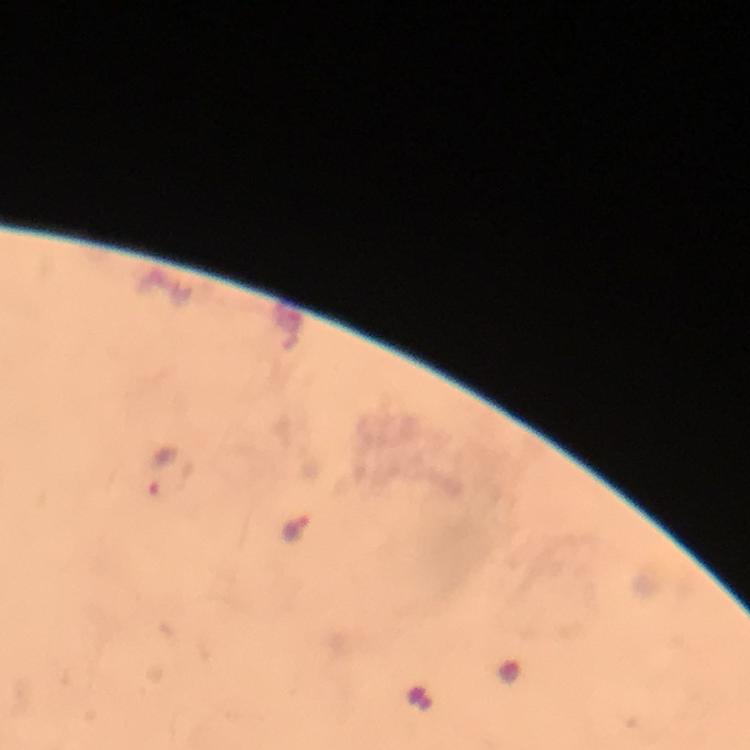

Approximate centers as {x, y} in pixels.
Summary:
  - Plasmodium parasite locations: {168, 474}, {298, 534}
  - Context: from a malaria diagnostic workup
  - Capture: smartphone camera through the microscope
  - Image size: 750×750 pixels
  - Magnification: 100x
  - Stain: Giemsa
  - Preparation: thick smear
  - Cropped from: one field of view
  - Immersion oil: applied